Report the malaria status of this cell.
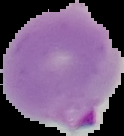
Parasitized.

From a thin blood film. The area outside the segmented cell region is set to black. Image is 124×136 pixels.